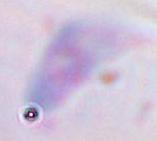

magnification = 1000x
modality = micrograph
identification = Toxoplasma gondii